Give the extent of all Plasmodium malariae-infected red blood cells.
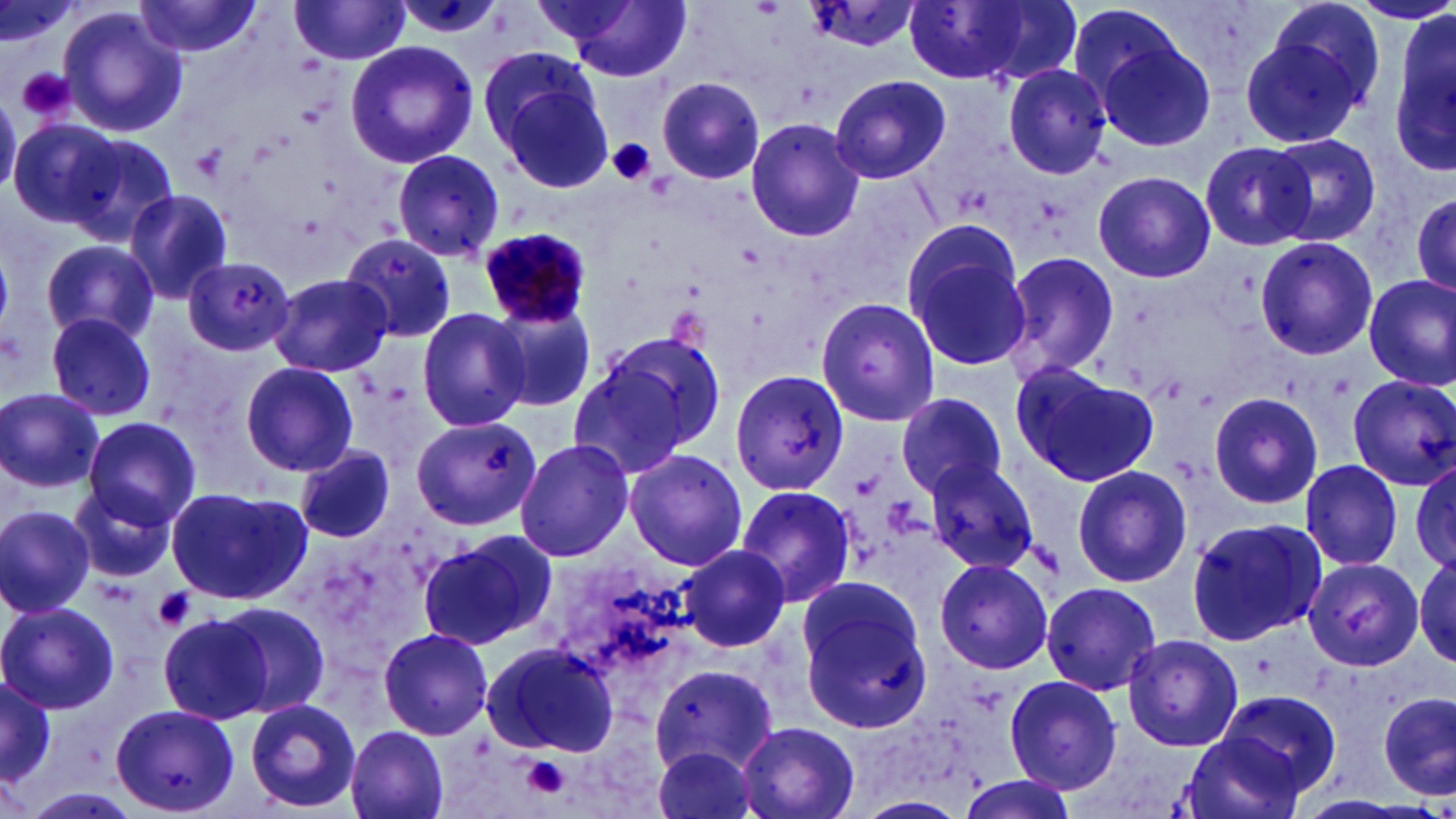
Approximate bounding boxes as [x1, y1, x2, y2] in pixels.
Plasmodium malariae-infected red blood cells: [479, 226, 596, 330].

slide_level_diagnosis: Plasmodium malariae
preparation: thin blood film
uninfected_red_blood_cell_locations: 'approximate bounding boxes as [x1, y1, x2, y2] in pixels: [554, 0, 693, 81], [3, 1, 74, 53], [134, 1, 263, 59], [902, 1, 1040, 83], [962, 1, 1084, 87], [289, 2, 413, 65], [800, 2, 926, 52], [59, 5, 188, 138], [1242, 10, 1376, 146], [1389, 10, 1456, 181], [1088, 22, 1216, 153], [343, 40, 480, 170], [1000, 63, 1114, 178], [491, 68, 615, 194], [830, 75, 952, 183], [657, 77, 765, 185], [9, 117, 119, 230], [746, 118, 866, 241], [64, 133, 178, 246], [1268, 134, 1380, 245], [1199, 141, 1317, 251], [390, 148, 506, 262], [1092, 170, 1216, 283], [1408, 187, 1456, 304], [124, 188, 234, 305], [903, 227, 1033, 373], [340, 232, 458, 345], [42, 238, 160, 347], [1254, 238, 1379, 360], [998, 249, 1121, 384], [181, 257, 296, 357], [271, 273, 392, 377], [1362, 274, 1456, 390], [815, 297, 942, 427], [489, 302, 596, 413], [415, 305, 535, 432], [45, 312, 157, 421], [571, 332, 726, 473], [240, 361, 360, 477], [1009, 361, 1156, 488], [728, 366, 849, 497], [1347, 375, 1456, 490], [0, 388, 104, 491], [1208, 390, 1322, 510], [895, 391, 1009, 499], [82, 414, 201, 526], [410, 416, 543, 531], [514, 439, 633, 563], [296, 445, 396, 543], [624, 448, 747, 571], [923, 459, 1041, 574], [1299, 459, 1404, 570], [1411, 462, 1456, 572], [1071, 465, 1193, 587], [70, 481, 180, 585], [734, 484, 857, 607], [166, 486, 310, 606], [0, 505, 96, 618], [1184, 516, 1325, 648], [418, 531, 556, 650], [679, 545, 794, 653], [1414, 556, 1455, 669], [933, 557, 1055, 674], [1303, 557, 1424, 671], [796, 577, 931, 731], [1040, 580, 1163, 697], [1, 600, 118, 714], [214, 601, 331, 717], [158, 614, 273, 720], [377, 625, 495, 741], [1122, 632, 1244, 752], [480, 640, 620, 758], [655, 658, 781, 770], [1, 674, 54, 788], [1004, 674, 1121, 791], [1214, 689, 1344, 802], [1379, 691, 1455, 801], [244, 698, 362, 812], [110, 703, 239, 817], [734, 720, 860, 819], [345, 725, 450, 819], [1181, 730, 1307, 819], [649, 745, 762, 819], [955, 774, 1078, 819], [851, 794, 969, 818]'
magnification: 1000x
stain: May-Grünwald-Giemsa
modality: light microscopy
field_of_view: single
platelet_locations: 'approximate bounding boxes as [x1, y1, x2, y2] in pixels: [16, 66, 76, 123], [607, 138, 657, 187], [151, 587, 195, 631], [521, 756, 572, 800]'
image_size: 1456×819 pixels